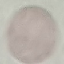
Result: no malaria parasites seen. Thin blood film. Giemsa stain. Automatically extracted cell patch, resized to 64 × 64 pixels. Photographed with a smartphone camera at the microscope eyepiece.